Comment on the morphology of the erythrocytes.
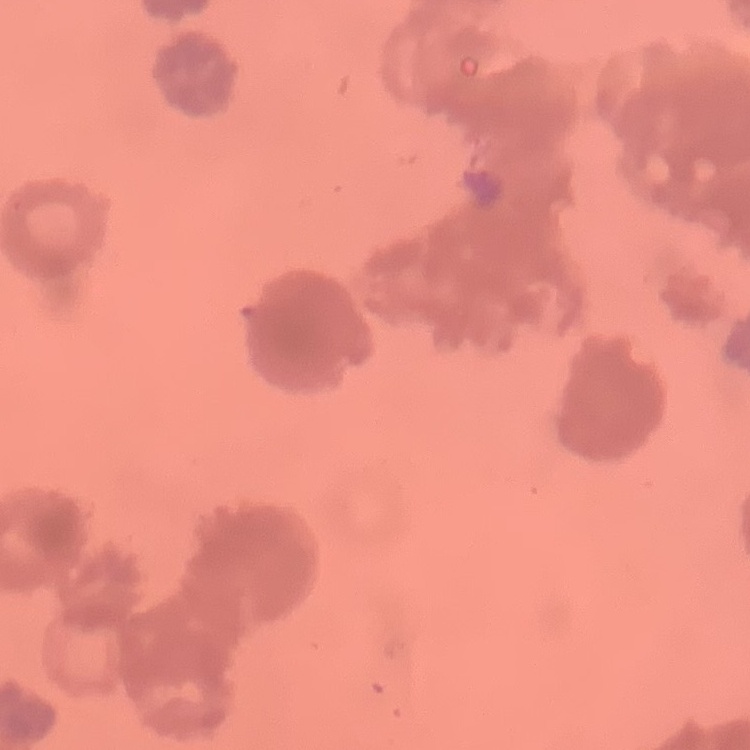

Rouleaux formation.

stain: Field's or Giemsa
image_type: square crop of a larger photomicrograph
preparation: thin peripheral smear